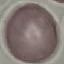

Summary:
  - Malaria status: uninfected
  - Image type: cell patch, automatically extracted from a larger field of view and resized to 64 × 64 pixels
  - Preparation: thin smear
  - Capture: smartphone through the microscope eyepiece
  - Stain: Giemsa